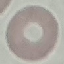 Malaria status: uninfected. Giemsa-stained preparation. Cell patch, automatically extracted from a larger field of view and resized to 64 × 64 pixels. Photographed with a smartphone camera at the microscope eyepiece. Thin blood film.